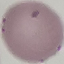

Summary:
  - Result: negative for malaria parasites
  - Image type: automatically extracted cell patch, resized to 64 × 64 pixels
  - Capture: smartphone camera at the microscope eyepiece
  - Stain: Giemsa
  - Preparation: thin blood smear